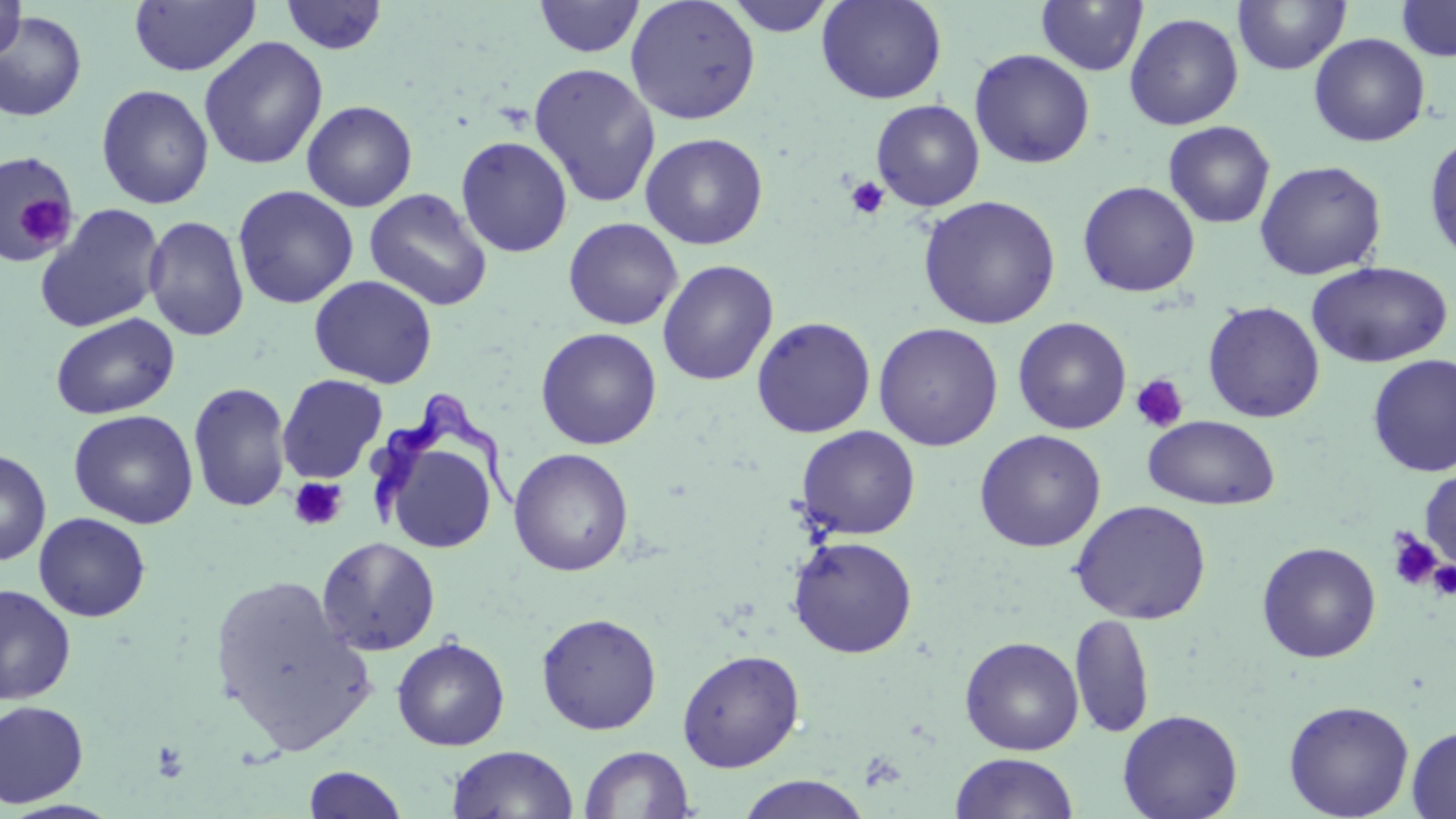
slide-level diagnosis = Trypanosoma brucei
platelet locations = approximate bounding boxes as (x1, y1, x2, y2) in pixels: (845, 176, 890, 220), (19, 193, 74, 253), (1131, 374, 1189, 433), (289, 477, 347, 531), (1386, 530, 1442, 591), (1428, 560, 1456, 599), (151, 739, 190, 783)
stain = May-Grünwald-Giemsa
field of view = single
magnification = 1000x
Trypanosoma brucei locations = approximate bounding boxes as (x1, y1, x2, y2) in pixels: (366, 382, 525, 533)
uninfected red blood cell locations = approximate bounding boxes as (x1, y1, x2, y2) in pixels: (0, 0, 26, 62), (128, 0, 260, 77), (532, 0, 644, 58), (625, 0, 761, 125), (723, 0, 838, 37), (817, 0, 947, 105), (1396, 0, 1456, 61), (279, 1, 389, 55), (1035, 1, 1149, 76), (1232, 1, 1351, 75), (0, 11, 87, 122), (1124, 12, 1244, 130), (1308, 33, 1430, 147), (198, 36, 329, 170), (969, 49, 1095, 169), (527, 62, 661, 208), (96, 84, 214, 209), (871, 99, 985, 211), (301, 100, 418, 212), (1163, 121, 1276, 228), (640, 132, 769, 250), (1424, 132, 1456, 266), (455, 136, 573, 258), (0, 151, 78, 264), (1254, 159, 1387, 280), (1077, 180, 1200, 297), (232, 185, 359, 309), (364, 188, 493, 311), (917, 194, 1061, 330), (34, 202, 166, 333), (143, 214, 250, 341), (563, 217, 683, 330), (657, 259, 779, 386), (1306, 261, 1453, 368), (309, 274, 438, 389), (1202, 301, 1325, 423), (50, 312, 180, 420), (751, 315, 877, 438), (1012, 316, 1131, 434), (873, 322, 1003, 451), (535, 327, 662, 450), (1367, 354, 1456, 477), (277, 374, 388, 484), (188, 381, 292, 513), (68, 410, 198, 528), (1143, 415, 1281, 510), (374, 425, 502, 556), (795, 425, 921, 539), (973, 429, 1107, 553), (0, 448, 51, 566), (508, 448, 634, 577), (1419, 469, 1456, 571), (1070, 499, 1212, 625), (33, 512, 151, 622), (787, 535, 918, 658), (316, 536, 441, 656), (1256, 541, 1381, 663), (208, 573, 375, 753), (0, 585, 77, 705), (536, 612, 662, 735), (1070, 613, 1154, 739), (960, 635, 1085, 756), (391, 636, 510, 750), (677, 649, 805, 773), (1283, 699, 1415, 818), (0, 700, 89, 807), (1117, 709, 1243, 819), (1407, 725, 1456, 818), (446, 744, 578, 819), (579, 745, 695, 818), (950, 752, 1078, 819), (303, 765, 409, 818), (736, 775, 871, 819)
preparation = thin blood smear
modality = optical microscopy
image size = 1456×819 pixels